Give the location of every parasitized red blood cell.
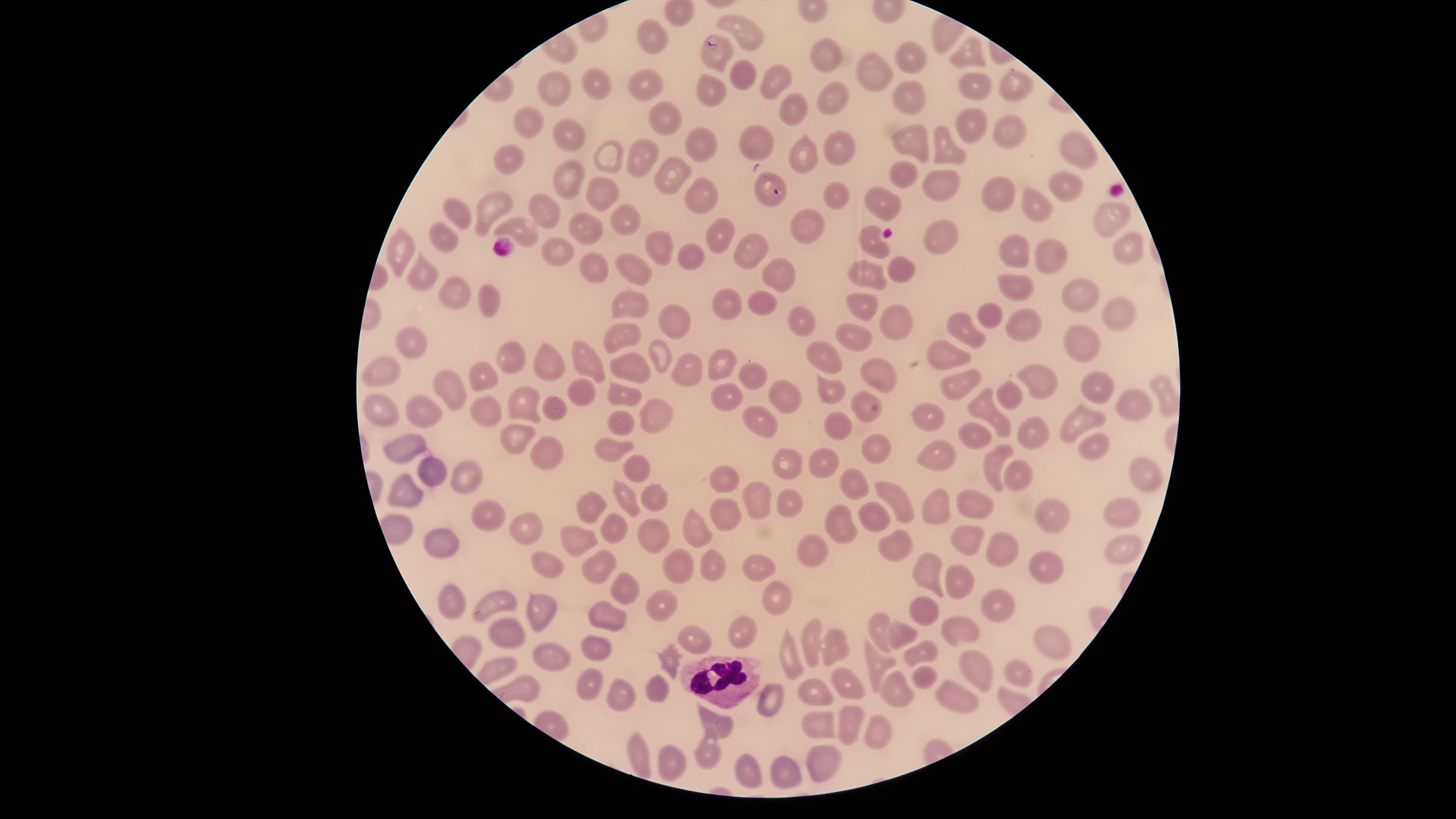
Approximate marker points, in pixels from the top-left corner.
Parasitized red blood cells: (x=713, y=43), (x=772, y=196).

Approximate marker points, in pixels from the top-left corner.
Summary:
  - White blood cells: (x=720, y=680)
  - Uninfected red blood cells: (x=746, y=30), (x=650, y=31), (x=908, y=45), (x=823, y=48), (x=972, y=51), (x=739, y=71), (x=873, y=71), (x=969, y=81), (x=1009, y=81), (x=595, y=83), (x=772, y=83), (x=644, y=86), (x=557, y=87), (x=710, y=87), (x=830, y=102), (x=910, y=104), (x=785, y=111), (x=669, y=117), (x=530, y=119), (x=971, y=122), (x=1009, y=129), (x=562, y=132), (x=757, y=141), (x=910, y=141), (x=703, y=142), (x=839, y=146), (x=1074, y=147), (x=942, y=149), (x=806, y=153), (x=602, y=155), (x=636, y=155), (x=509, y=157), (x=670, y=174), (x=900, y=175), (x=570, y=179), (x=937, y=183), (x=1069, y=183), (x=839, y=189), (x=700, y=190), (x=599, y=191), (x=996, y=194), (x=884, y=195), (x=484, y=205), (x=542, y=205), (x=457, y=208), (x=1036, y=209), (x=1107, y=217), (x=584, y=222), (x=627, y=223), (x=811, y=224), (x=522, y=225), (x=444, y=231), (x=719, y=232), (x=938, y=233), (x=870, y=241), (x=1124, y=243), (x=395, y=249), (x=656, y=249), (x=549, y=252), (x=1050, y=252), (x=754, y=253), (x=1019, y=253), (x=692, y=254), (x=593, y=267), (x=901, y=268), (x=777, y=269), (x=870, y=269), (x=639, y=270), (x=417, y=276), (x=1018, y=283), (x=1079, y=290), (x=452, y=294), (x=766, y=297), (x=859, y=301), (x=487, y=302), (x=724, y=304), (x=631, y=305), (x=1118, y=310), (x=801, y=312), (x=992, y=318), (x=671, y=319), (x=893, y=319), (x=967, y=324), (x=1020, y=325), (x=620, y=333), (x=1084, y=335), (x=858, y=338), (x=417, y=344), (x=823, y=354), (x=662, y=355), (x=509, y=356), (x=942, y=356), (x=586, y=357), (x=545, y=360), (x=717, y=364), (x=632, y=367), (x=383, y=368), (x=879, y=368), (x=483, y=369), (x=747, y=369), (x=1033, y=374), (x=958, y=379), (x=1104, y=382), (x=577, y=387), (x=455, y=388), (x=830, y=392), (x=614, y=393), (x=1007, y=393), (x=783, y=395), (x=733, y=400), (x=859, y=400), (x=526, y=401), (x=1133, y=404), (x=554, y=407), (x=984, y=407), (x=382, y=408), (x=416, y=410), (x=484, y=410), (x=925, y=413), (x=658, y=417), (x=618, y=422), (x=764, y=422), (x=1086, y=424), (x=843, y=425), (x=1035, y=426), (x=974, y=432), (x=513, y=436), (x=873, y=438), (x=404, y=444), (x=609, y=444), (x=542, y=447), (x=1086, y=448), (x=936, y=454), (x=994, y=462), (x=821, y=465), (x=638, y=467), (x=792, y=468), (x=1144, y=469), (x=426, y=470), (x=465, y=470), (x=726, y=475), (x=1017, y=478), (x=857, y=487), (x=900, y=494), (x=406, y=495), (x=625, y=496), (x=649, y=497), (x=761, y=500), (x=589, y=502), (x=728, y=503), (x=791, y=503), (x=936, y=505), (x=975, y=507), (x=1121, y=510), (x=487, y=515), (x=876, y=515), (x=1058, y=515), (x=844, y=522), (x=607, y=523), (x=522, y=525), (x=698, y=529), (x=969, y=534), (x=649, y=535), (x=444, y=537), (x=578, y=538), (x=894, y=543), (x=1004, y=546), (x=825, y=550), (x=1116, y=552), (x=546, y=559), (x=711, y=560), (x=596, y=562), (x=677, y=562), (x=756, y=567), (x=1049, y=569), (x=925, y=572), (x=962, y=579), (x=622, y=582), (x=774, y=593), (x=449, y=594), (x=658, y=600), (x=498, y=601), (x=1003, y=601), (x=539, y=603), (x=922, y=609), (x=612, y=619), (x=741, y=627), (x=511, y=628), (x=879, y=628), (x=957, y=628), (x=901, y=636), (x=697, y=638), (x=812, y=640), (x=1056, y=641), (x=839, y=644), (x=604, y=648), (x=924, y=651), (x=550, y=654), (x=669, y=655), (x=789, y=655), (x=976, y=663), (x=875, y=664), (x=1018, y=673), (x=924, y=674), (x=842, y=684), (x=661, y=686), (x=585, y=687), (x=813, y=687), (x=894, y=689), (x=627, y=696), (x=954, y=698), (x=771, y=700), (x=715, y=722), (x=849, y=722), (x=817, y=723), (x=876, y=727), (x=636, y=744), (x=707, y=750), (x=676, y=760), (x=815, y=760), (x=744, y=772), (x=786, y=777)
  - Preparation: thin blood smear
  - Visible region: circular
  - Capture: smartphone photograph through the microscope eyepiece
  - Image size: 1456×819 pixels
  - Field of view: single
  - Stain: Giemsa
  - Species: Plasmodium falciparum